Identify the parasite.
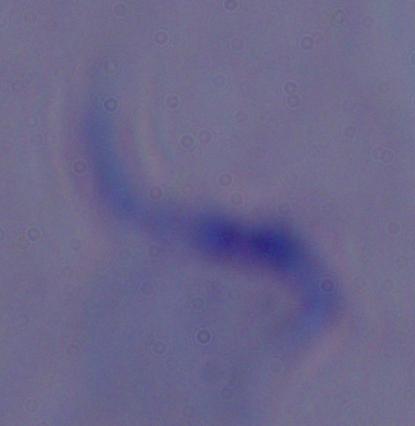

A trypanosome.

magnification: 1000x
modality: photomicrograph